State which cell type is depicted.
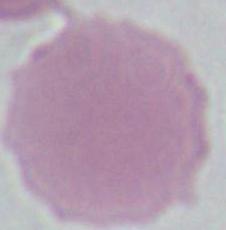
This is an erythrocyte.

Micrograph. Captured at 1000x magnification.